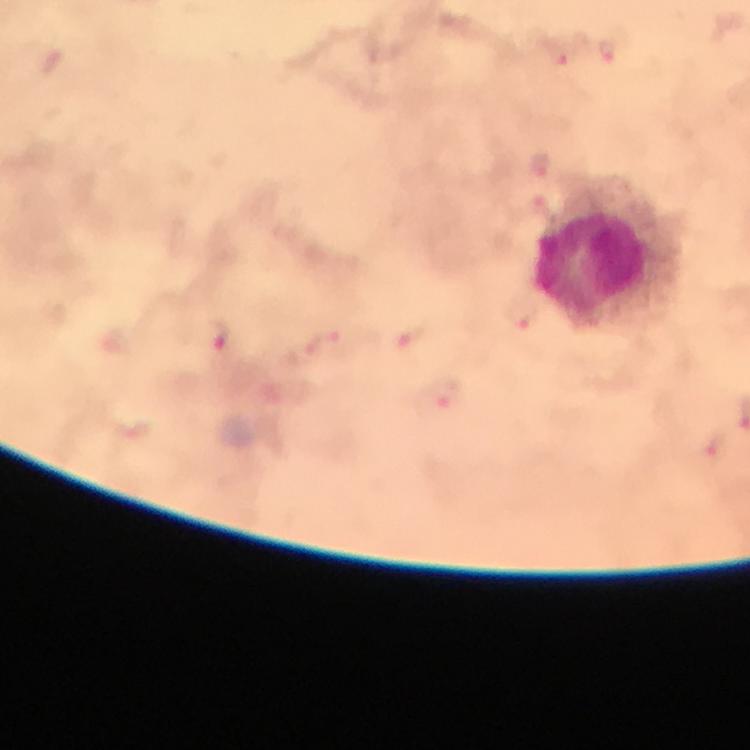
Approximate centers as (x, y) in pixels. Malaria parasite locations: (559, 55), (609, 55), (541, 165), (543, 209), (519, 314), (222, 335), (413, 336), (327, 343), (445, 397), (713, 446). Leukocyte locations: (598, 271). Image is 750×750 pixels. Giemsa stain. Immersion oil was used. 100x magnification. From a malaria diagnostic workup. Photographed through the microscope with a smartphone camera. Thick blood film. Cropped region of a single field of view.